State which parasite is depicted.
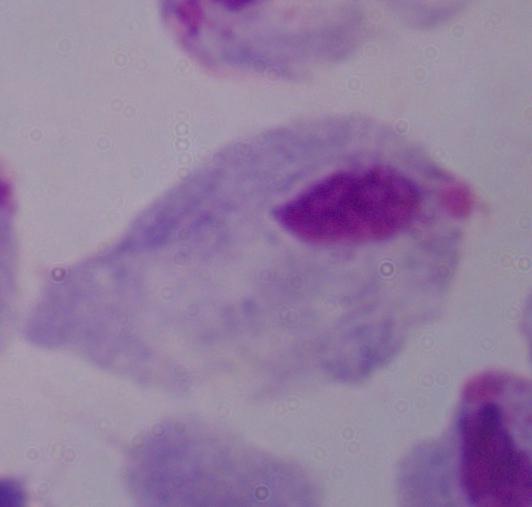

A trichomonad.

modality = micrograph
magnification = 1000x